Report the malaria status of this cell.
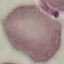

It is uninfected.

{
  "image_type": "automatically extracted cell patch, resized to 64 × 64 pixels",
  "capture": "smartphone through the microscope eyepiece",
  "preparation": "thin smear",
  "stain": "Giemsa"
}